Point out each malaria parasite.
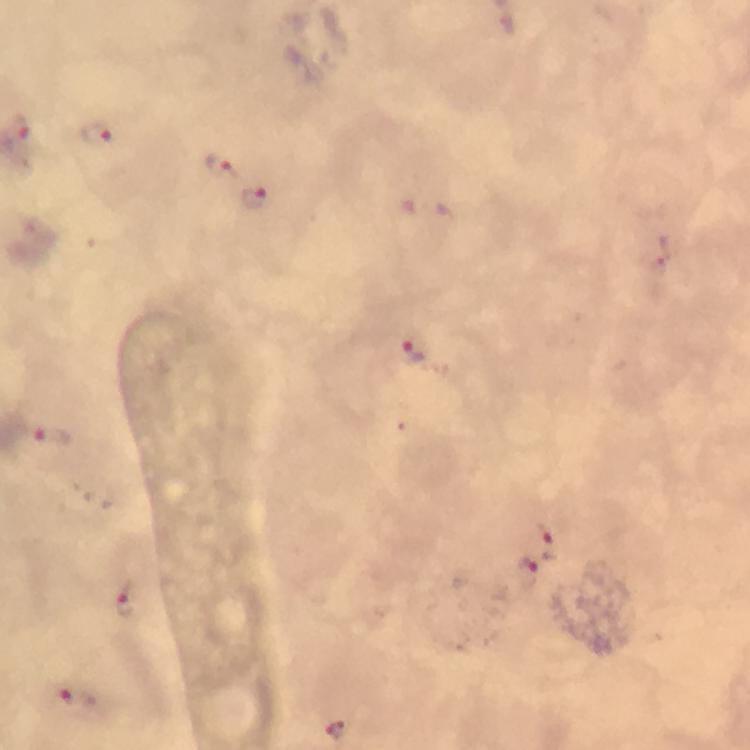
Approximate centers as [x, y] in pixels.
Malaria parasites: [94, 135], [219, 167], [253, 195], [656, 251], [410, 350], [50, 435], [546, 541], [525, 574], [128, 599], [78, 699], [338, 730].

At 100x magnification. Photographed through the microscope with a smartphone camera. From a malaria diagnostic workup. Cropped region of a single field of view. Image is 750×750 pixels. Thick blood film. Giemsa-stained preparation. Immersion oil was used.